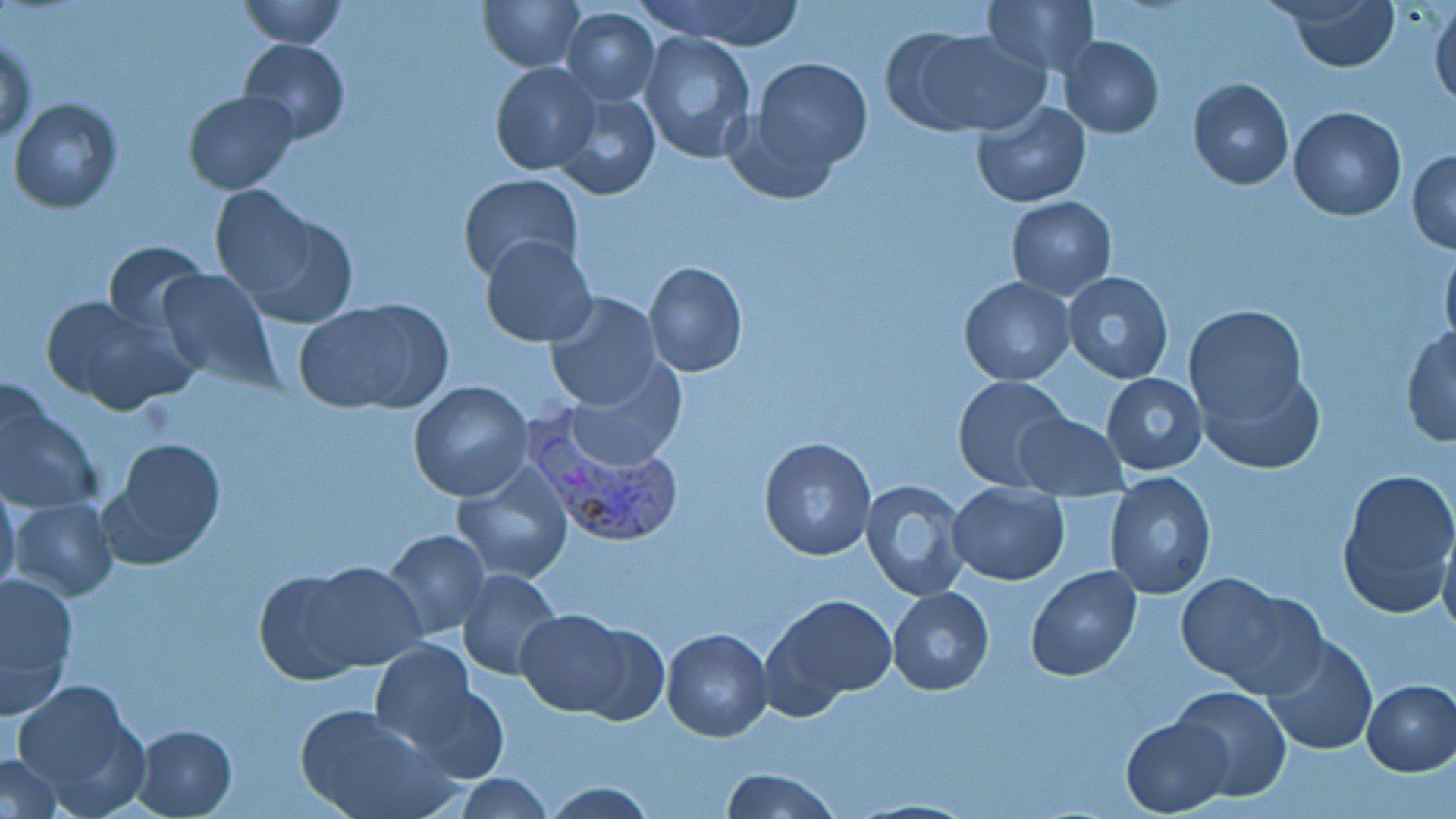
Approximate bounding boxes as [x1, y1, x2, y2] in pixels. Plasmodium vivax-infected red blood cell locations: [525, 409, 687, 555]. Uninfected red blood cell locations: [239, 0, 345, 48], [479, 0, 585, 72], [636, 0, 808, 48], [1280, 0, 1400, 72], [981, 1, 1099, 77], [1430, 2, 1456, 111], [561, 7, 660, 105], [895, 27, 1046, 136], [640, 31, 757, 165], [1060, 35, 1164, 138], [1, 37, 38, 146], [238, 37, 349, 144], [751, 57, 873, 173], [491, 62, 600, 176], [1187, 77, 1294, 190], [183, 90, 299, 195], [552, 90, 660, 201], [9, 99, 123, 215], [970, 101, 1092, 206], [1288, 106, 1407, 221], [1407, 148, 1456, 254], [457, 174, 582, 282], [210, 185, 329, 313], [1006, 195, 1117, 300], [479, 236, 596, 347], [101, 239, 210, 336], [1440, 241, 1456, 355], [643, 261, 747, 378], [156, 268, 279, 389], [1061, 273, 1175, 384], [959, 277, 1075, 386], [544, 292, 664, 413], [42, 295, 191, 416], [294, 298, 448, 414], [1183, 304, 1309, 430], [1401, 326, 1455, 447], [566, 358, 687, 469], [1196, 365, 1324, 476], [1101, 372, 1208, 476], [951, 374, 1072, 491], [407, 382, 534, 502], [0, 389, 100, 515], [1013, 413, 1127, 500], [758, 436, 877, 561], [103, 437, 227, 567], [452, 464, 573, 584], [1335, 469, 1455, 619], [1103, 475, 1216, 600], [860, 479, 972, 601], [0, 483, 22, 598], [946, 485, 1069, 586], [10, 498, 118, 599], [1438, 522, 1456, 641], [381, 529, 490, 641], [296, 562, 429, 673], [1026, 565, 1141, 681], [0, 568, 78, 711], [457, 568, 565, 680], [254, 569, 374, 685], [1175, 572, 1292, 684], [887, 586, 994, 695], [764, 594, 896, 711], [517, 609, 638, 716], [661, 627, 773, 742], [1263, 634, 1376, 756], [369, 639, 479, 748], [11, 678, 149, 815], [1360, 678, 1456, 776], [1171, 683, 1291, 802], [406, 686, 510, 783], [296, 704, 448, 819], [1121, 717, 1230, 816], [132, 724, 237, 816], [1, 753, 63, 818], [721, 767, 839, 819], [450, 774, 556, 818], [539, 780, 660, 818], [851, 796, 980, 818]. Slide-level diagnosis: Plasmodium vivax. Optical microscopy. Image is 1456×819 pixels. May-Grünwald-Giemsa-stained preparation. Thin blood smear. 1000x magnification. One field of a larger specimen.